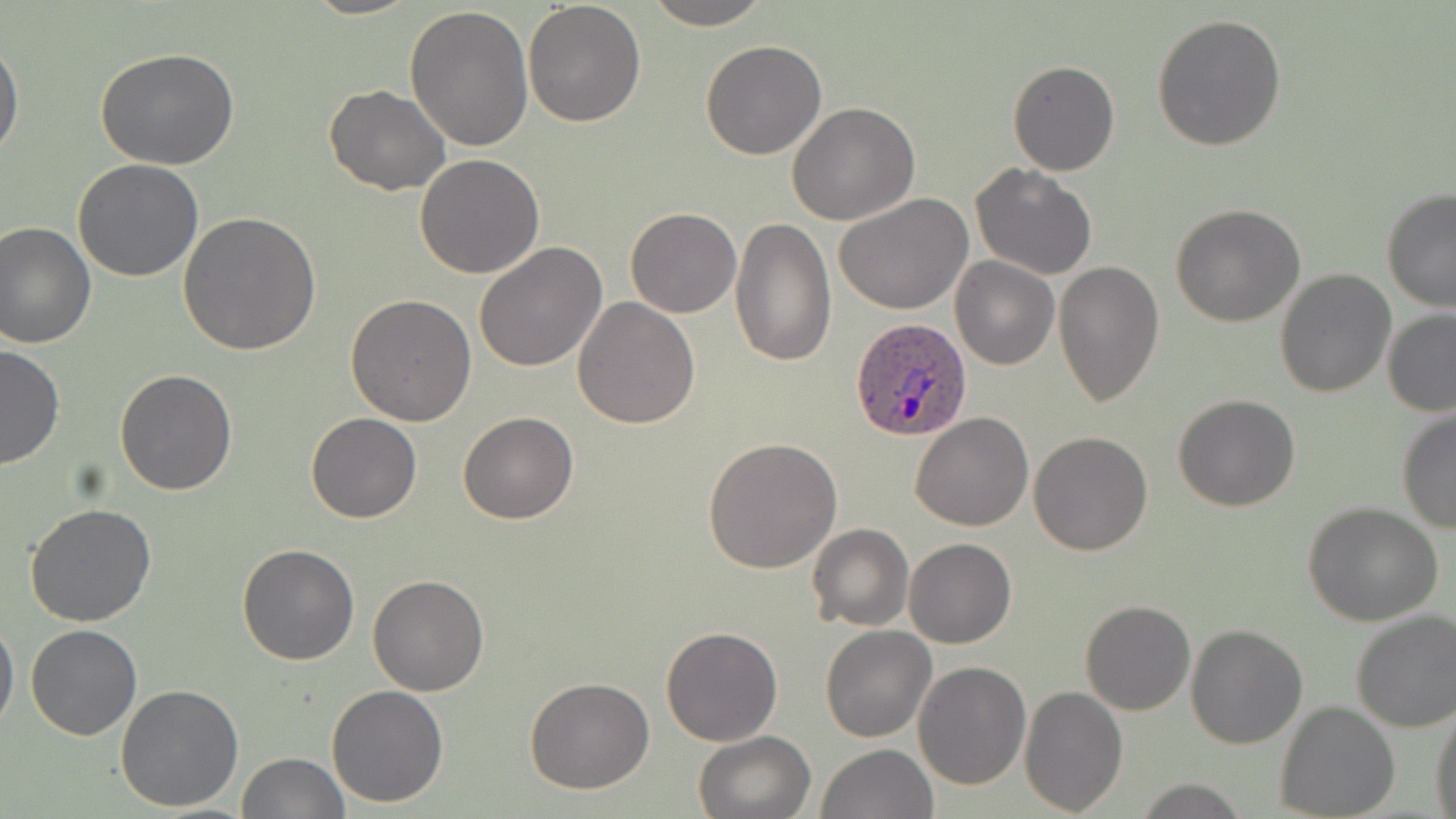

Approximate bounding boxes as (x1,y1)-(x2,y2) corner pairs in pixels. Plasmodium ovale-infected red blood cell locations: (849,318)-(973,443). Uninfected red blood cell locations: (302,0)-(419,20), (641,0)-(771,29), (523,1)-(647,127), (404,5)-(533,151), (1151,13)-(1287,151), (1,36)-(24,162), (700,40)-(827,160), (96,49)-(242,170), (1008,60)-(1120,175), (323,85)-(450,196), (787,102)-(919,224), (415,154)-(546,279), (72,159)-(204,282), (969,163)-(1098,280), (1380,189)-(1456,312), (834,195)-(973,315), (1171,204)-(1305,326), (625,207)-(741,318), (178,213)-(320,358), (730,216)-(838,366), (0,220)-(98,349), (473,242)-(608,373), (951,257)-(1059,370), (1053,261)-(1164,408), (1275,268)-(1396,397), (347,295)-(477,426), (572,296)-(700,429), (1382,309)-(1456,417), (0,343)-(65,469), (114,370)-(238,495), (1172,394)-(1301,512), (1397,411)-(1455,534), (305,412)-(421,523), (459,412)-(578,523), (911,413)-(1034,531), (1027,431)-(1152,555), (703,438)-(844,574), (25,502)-(158,627), (1303,503)-(1444,626), (806,524)-(913,631), (903,537)-(1016,648), (236,544)-(360,665), (368,574)-(489,696), (1081,600)-(1195,715), (1350,609)-(1456,733), (0,615)-(19,738), (25,624)-(141,740), (820,625)-(936,742), (1186,626)-(1308,748), (660,627)-(784,746), (913,660)-(1030,789), (525,676)-(656,793), (113,683)-(243,813), (325,684)-(450,807), (1019,685)-(1128,815), (1275,701)-(1401,818), (1430,704)-(1456,819), (693,730)-(815,819), (816,744)-(938,819), (236,752)-(349,818). Slide-level diagnosis: Plasmodium ovale. Captured at 1000x magnification. May-Grünwald-Giemsa-stained preparation. Optical microscopy. Image is 1456×819 pixels. Single field of view. Thin blood smear.